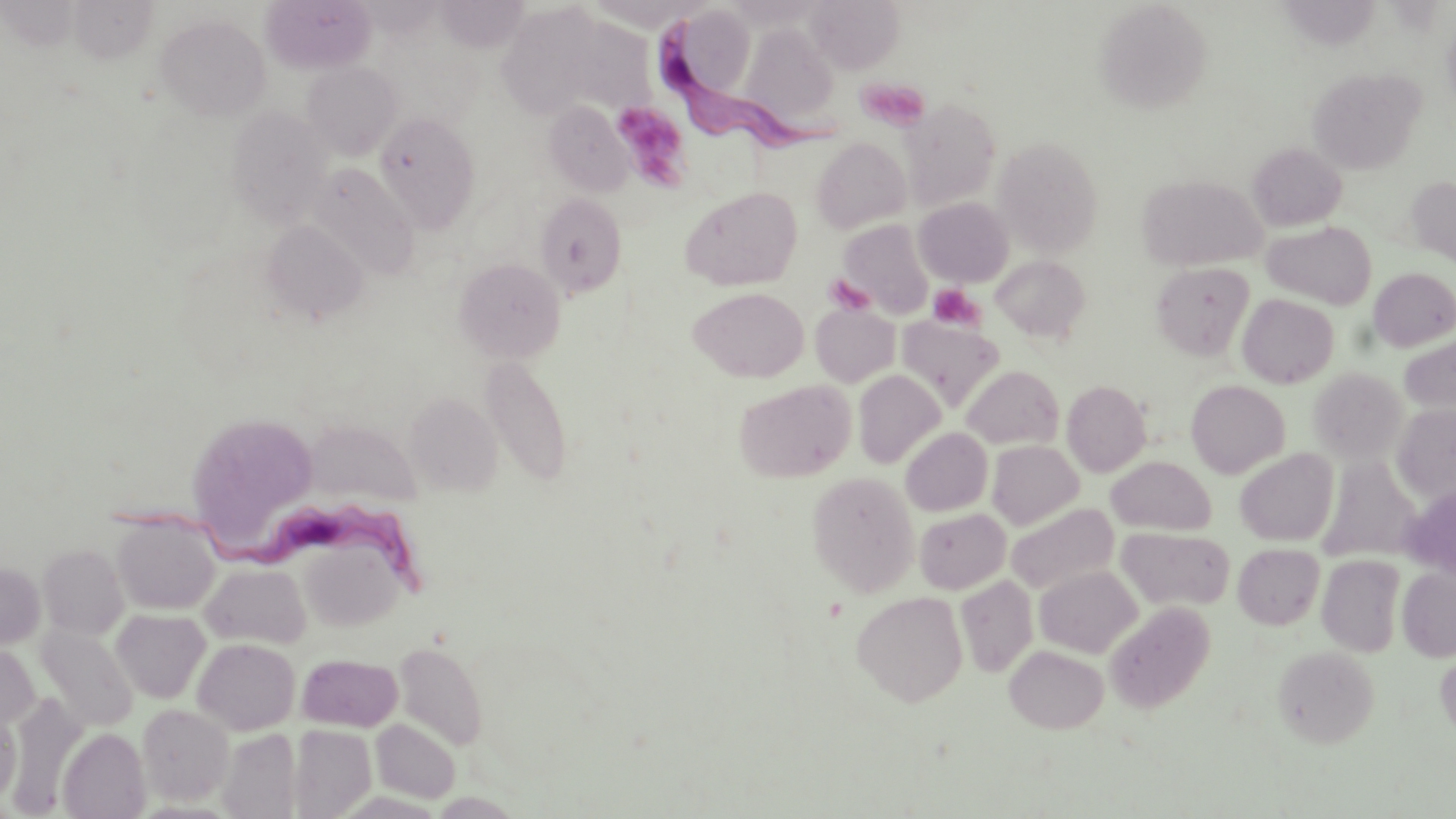

Approximate bounding boxes as (x1,y1)-(x2,y2) corner pairs in pixels. Platelet locations: (857,76)-(931,130), (609,100)-(694,191), (826,275)-(875,316), (929,285)-(983,332). Trypanosoma brucei locations: (656,14)-(851,155), (113,497)-(433,608). Uninfected red blood cell locations: (807,0)-(904,73), (262,1)-(375,73), (1095,2)-(1212,113), (682,5)-(760,92), (496,7)-(598,118), (155,14)-(271,120), (740,23)-(841,128), (302,61)-(403,159), (1308,68)-(1424,173), (903,98)-(1001,208), (544,102)-(633,196), (226,106)-(334,227), (374,112)-(480,231), (339,134)-(460,269), (811,137)-(912,233), (994,137)-(1104,254), (1248,143)-(1346,230), (306,162)-(420,280), (1137,175)-(1266,270), (1406,176)-(1456,266), (681,186)-(802,291), (534,193)-(627,296), (915,197)-(1014,286), (839,219)-(935,319), (260,220)-(369,325), (1262,220)-(1377,309), (992,255)-(1090,342), (453,257)-(566,362), (1151,262)-(1254,360), (1369,268)-(1456,351), (689,287)-(809,382), (1237,294)-(1339,388), (811,304)-(900,386), (897,318)-(1003,410), (1400,334)-(1456,419), (480,354)-(573,486), (962,365)-(1064,449), (1309,367)-(1407,464), (853,370)-(946,469), (734,379)-(856,483), (1062,380)-(1150,476), (1186,380)-(1290,478), (404,393)-(503,495), (1392,404)-(1456,504), (186,413)-(318,543), (304,418)-(422,507), (901,428)-(992,516), (987,441)-(1083,530), (1235,449)-(1338,545), (1318,455)-(1421,563), (1106,456)-(1216,535), (807,471)-(920,596), (1401,486)-(1456,579), (1006,502)-(1119,594), (914,508)-(1010,594), (111,513)-(221,615), (1118,527)-(1234,611), (298,536)-(406,631), (1233,543)-(1325,629), (38,545)-(127,639), (1317,554)-(1406,657), (0,561)-(45,649), (201,562)-(310,648), (1035,565)-(1141,657), (1397,566)-(1456,661), (956,576)-(1038,676), (851,590)-(968,706), (1104,601)-(1215,713), (111,609)-(210,703), (36,624)-(139,732), (193,638)-(301,734), (395,639)-(489,751), (0,643)-(40,729), (1005,644)-(1110,732), (1273,645)-(1380,747), (1435,646)-(1456,743), (296,653)-(404,731), (8,695)-(87,814), (137,703)-(234,805), (0,706)-(21,805), (371,718)-(461,803), (288,724)-(377,817), (58,727)-(151,818), (218,728)-(302,819). Slide-level diagnosis: Trypanosoma brucei. Optical microscopy. Image is 1456×819 pixels. Thin blood smear. Single field of view. Captured at 1000x magnification. May-Grünwald-Giemsa stain.